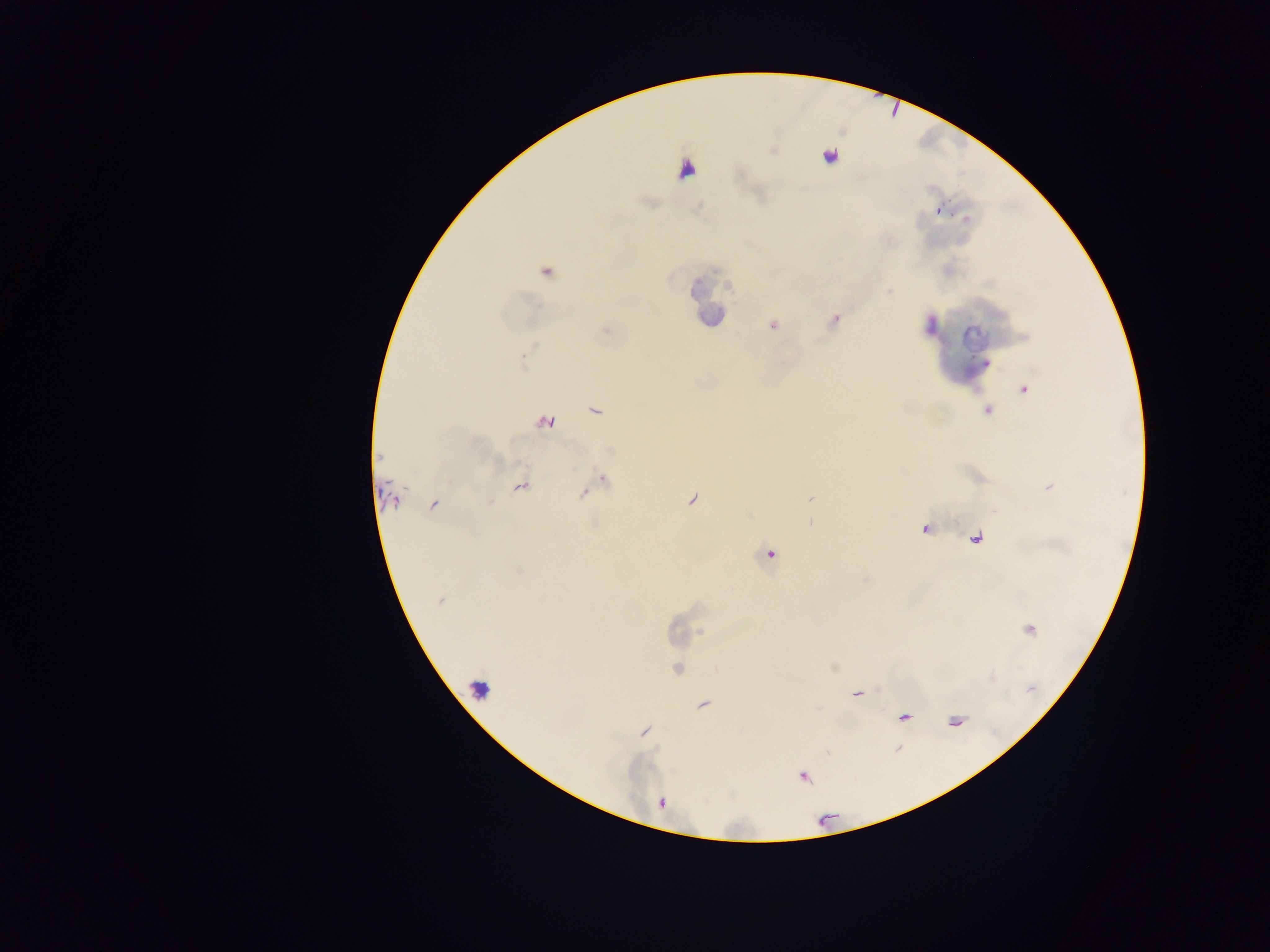 Approximate centers as [x, y] in pixels. Plasmodium parasite locations: [772, 151], [828, 156], [651, 203], [699, 206], [940, 214], [963, 216], [544, 271], [697, 285], [727, 286], [891, 292], [530, 299], [536, 305], [706, 315], [833, 319], [772, 325], [927, 326], [605, 328], [532, 348], [523, 357], [985, 364], [524, 365], [1026, 389], [593, 408], [987, 408], [546, 420], [608, 449], [379, 456], [603, 480], [521, 486], [582, 492], [810, 499], [692, 500], [389, 503], [490, 503], [434, 504], [770, 554], [519, 570], [864, 579], [440, 600], [676, 628], [701, 632], [676, 669], [857, 693], [704, 705], [906, 717], [646, 727], [644, 732], [639, 733], [899, 748], [828, 751], [804, 775]. Image is 1270×952 pixels. Sample from Ghana. Thick blood film. Photographed through a microscope with a mobile-phone camera. Single field of view.